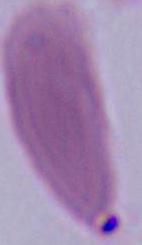

magnification = 1000x
identification = red blood cell
modality = micrograph